Identify the preparation type.
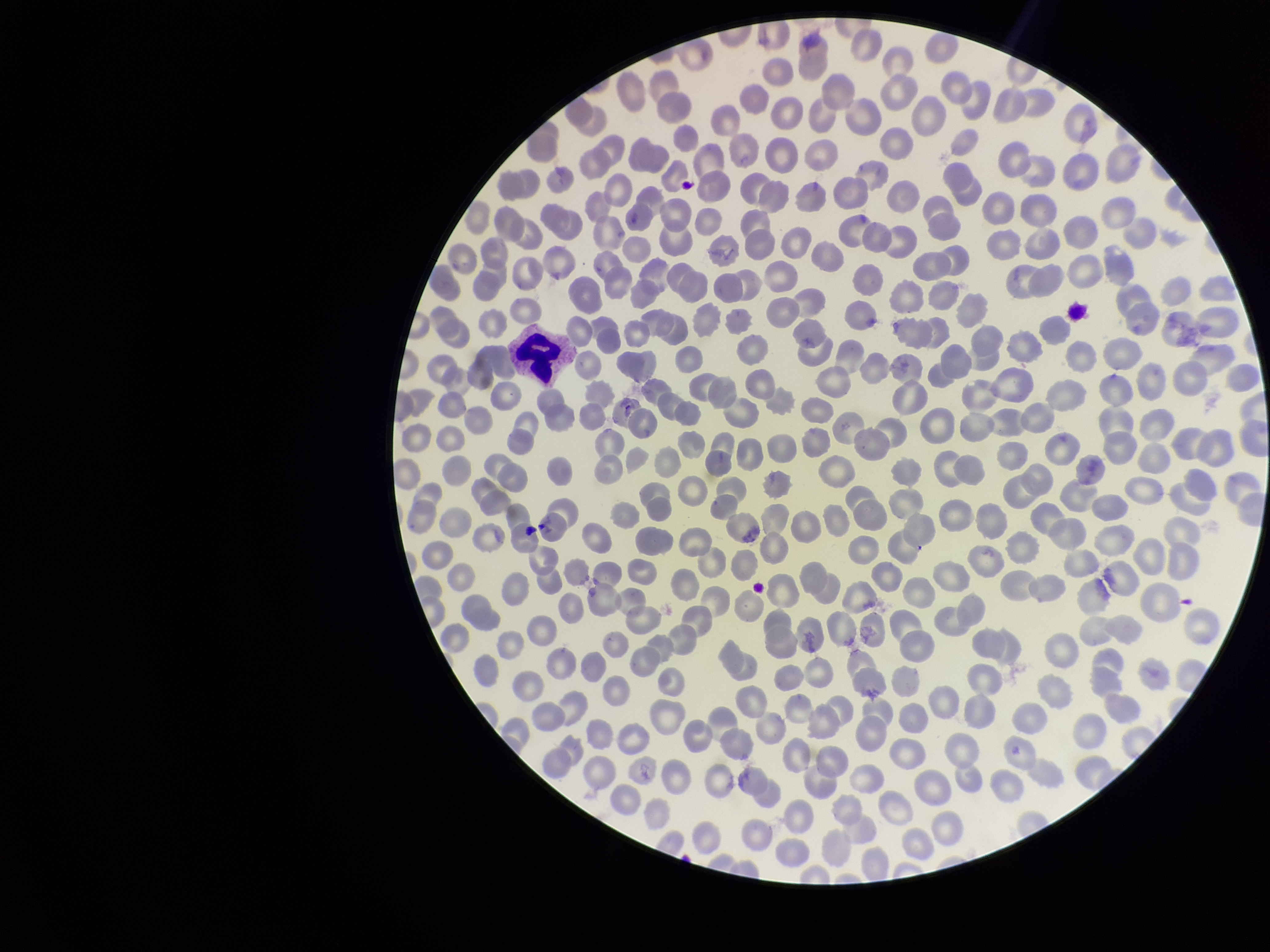

Thin.

Summary:
  - Capture: smartphone photograph through the microscope eyepiece
  - Field of view: single
  - Stain: Giemsa
  - Species reported for this patient: Plasmodium vivax
  - Red blood cell count: 309
  - Parasitized red blood cell count: 0
  - Image size: 1270×952 pixels
  - Parasitized red blood cells: none identified
  - Patient malaria status: positive